State which parasite is depicted.
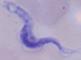

A trypanosome.

Summary:
  - Modality: micrograph
  - Magnification: 1000x